Report the malaria status of this cell.
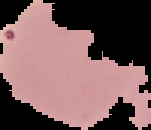
Uninfected.

Summary:
  - Image size: 151×130 pixels
  - Image type: segmented cell region with the area outside set to black
  - Preparation: thin blood smear